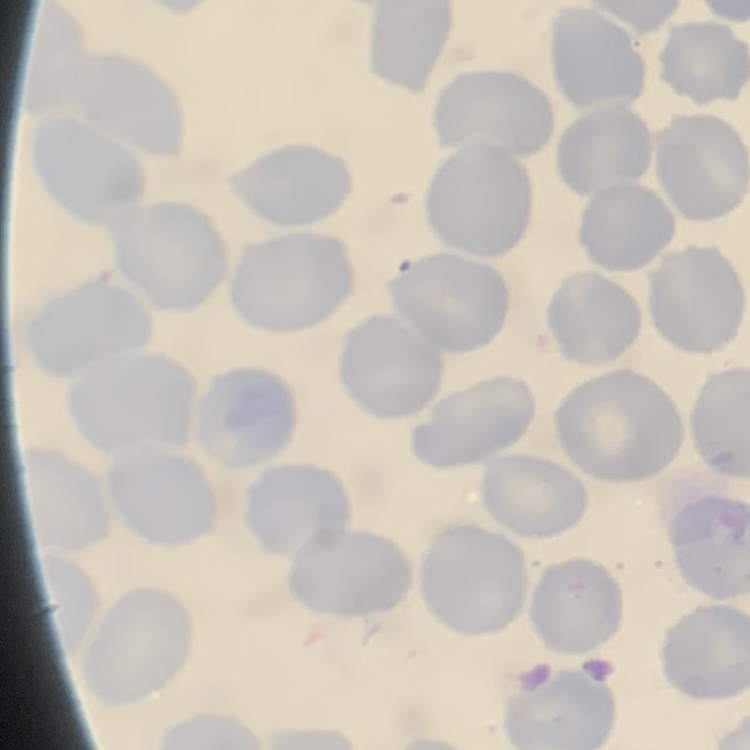

The red blood cells exhibit no rouleaux formation. Stained with either Field's or Giemsa. Thin peripheral smear. One tile cut from a larger photomicrograph.